Classify this cell by malaria status.
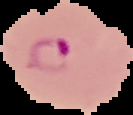
It is parasitized.

image size = 133×115 pixels
preparation = thin blood film
image type = segmented cell region with the area outside set to black